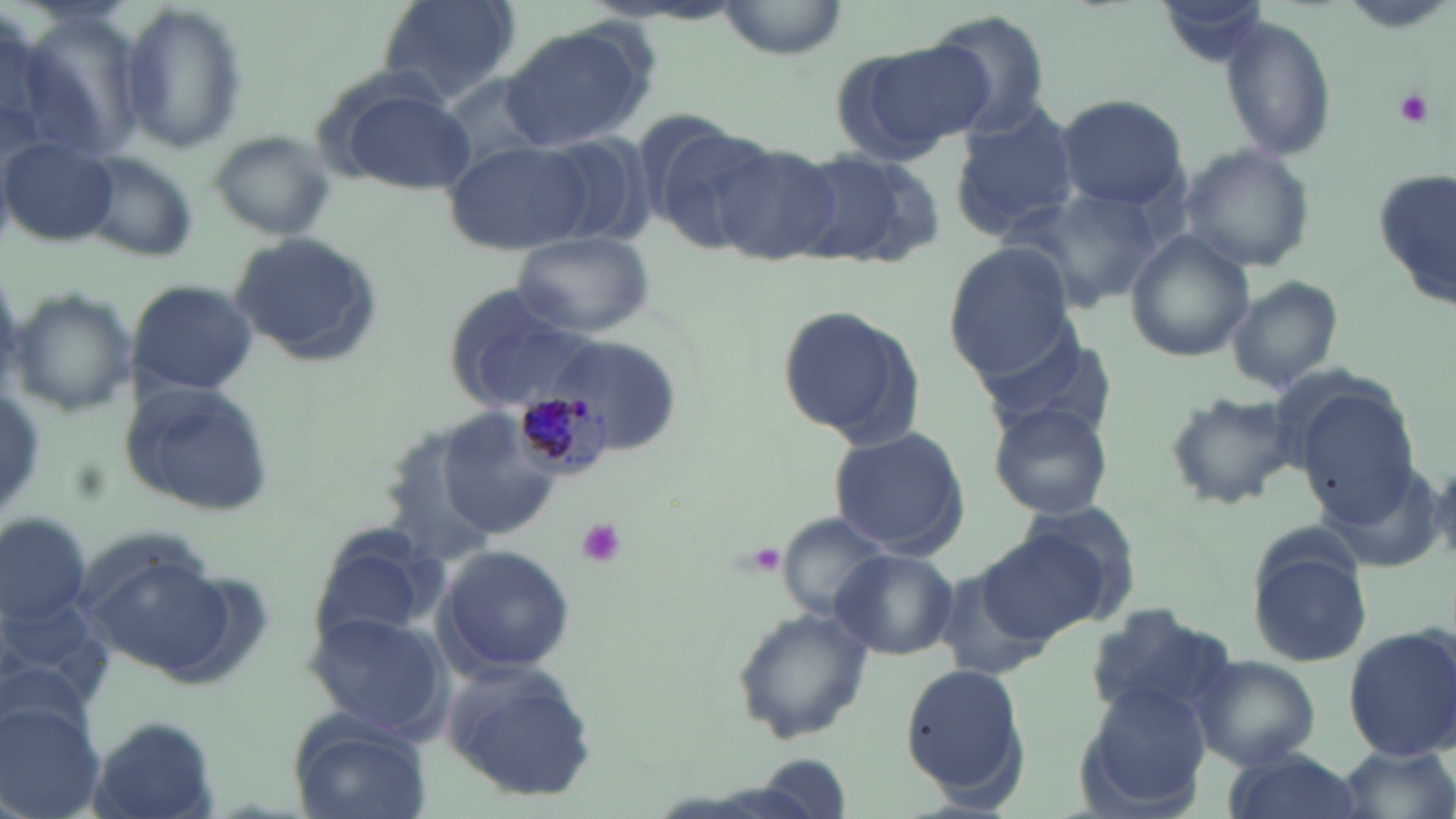

Approximate bounding boxes as (x1, y1, x2, y2) in pixels. Uninfected red blood cell locations: (374, 0, 521, 106), (710, 0, 850, 59), (1159, 0, 1271, 68), (119, 2, 247, 154), (921, 10, 1055, 138), (1218, 14, 1337, 160), (498, 21, 658, 155), (829, 37, 992, 163), (327, 82, 478, 197), (1055, 94, 1189, 209), (947, 105, 1081, 238), (643, 116, 776, 248), (209, 131, 336, 238), (537, 136, 655, 249), (1, 137, 121, 248), (445, 142, 594, 257), (1176, 144, 1317, 273), (713, 145, 840, 261), (793, 146, 940, 272), (77, 150, 199, 261), (1371, 170, 1455, 312), (1007, 187, 1164, 311), (512, 229, 654, 338), (230, 231, 381, 364), (1127, 231, 1254, 362), (943, 244, 1076, 379), (1226, 275, 1344, 395), (125, 278, 258, 397), (442, 286, 599, 410), (7, 287, 138, 420), (777, 301, 925, 448), (970, 322, 1115, 440), (552, 333, 682, 456), (117, 380, 278, 518), (1296, 390, 1420, 527), (1163, 391, 1301, 510), (987, 402, 1113, 519), (440, 409, 568, 541), (828, 426, 970, 558), (1022, 500, 1144, 612), (775, 511, 892, 619), (1, 514, 89, 628), (305, 525, 445, 657), (978, 529, 1108, 642), (435, 543, 576, 674), (1248, 543, 1374, 669), (831, 548, 958, 661), (82, 552, 233, 680), (934, 563, 1069, 683), (1083, 604, 1237, 724), (729, 605, 874, 745), (303, 611, 447, 739), (1341, 625, 1456, 757), (1190, 656, 1320, 768), (442, 660, 600, 798), (900, 661, 1030, 802), (1076, 681, 1212, 812), (0, 705, 107, 819), (285, 712, 433, 819), (83, 716, 222, 819), (1335, 742, 1455, 819), (1221, 749, 1364, 819). Plasmodium malariae-infected red blood cell locations: (516, 390, 605, 474). Platelet locations: (1395, 86, 1434, 126), (573, 518, 628, 568). Slide-level diagnosis: Plasmodium malariae. Single field of view. 1000x magnification. Optical microscopy. Thin blood smear. Image is 1456×819 pixels. May-Grünwald-Giemsa stain.